Locate Plasmodium parasites and leukocytes.
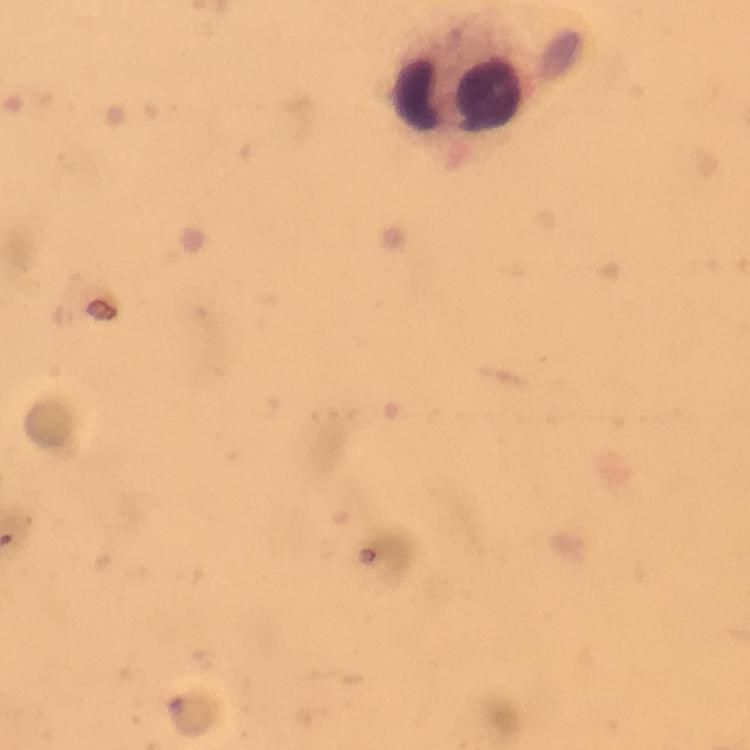
No Plasmodium parasites detected.
Approximate object centers, in pixels from the top-left corner.
Leukocytes: (x=461, y=99).

stain = Giemsa
immersion oil = applied
image size = 750×750 pixels
capture = smartphone photograph through a microscope
preparation = thick blood smear
cropped from = a single field of view
context = from a diagnostic examination for malaria
magnification = 100x